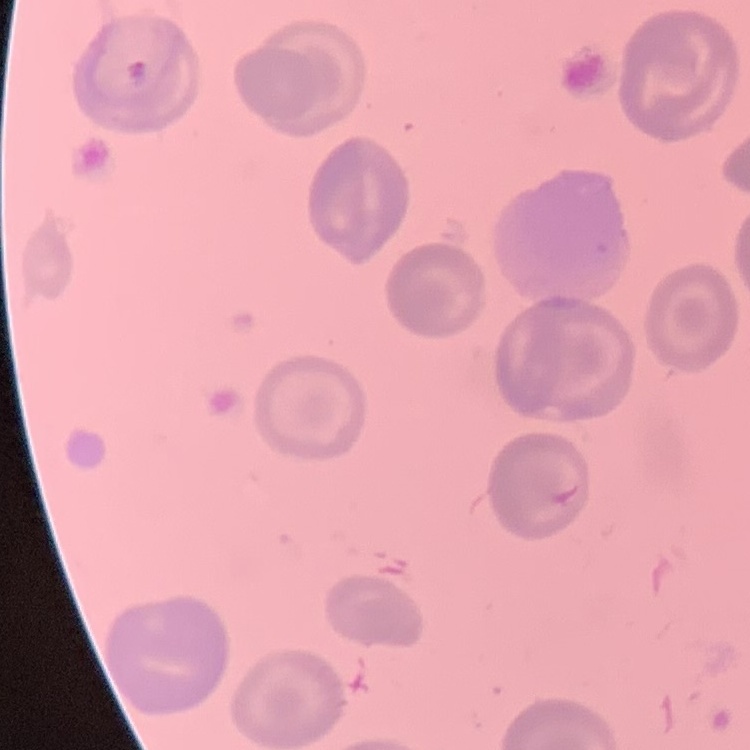
Summary:
  - Erythrocyte morphology: no rouleaux formation
  - Stain: Field's or Giemsa
  - Image type: square crop of a larger photomicrograph
  - Preparation: thin blood smear